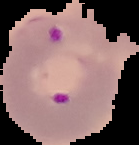

Summary:
  - Image size: 139×145 pixels
  - Image type: segmented cell region with the area outside set to black
  - Result: malaria parasites identified
  - Preparation: thin blood smear